Assess the morphology of the erythrocytes.
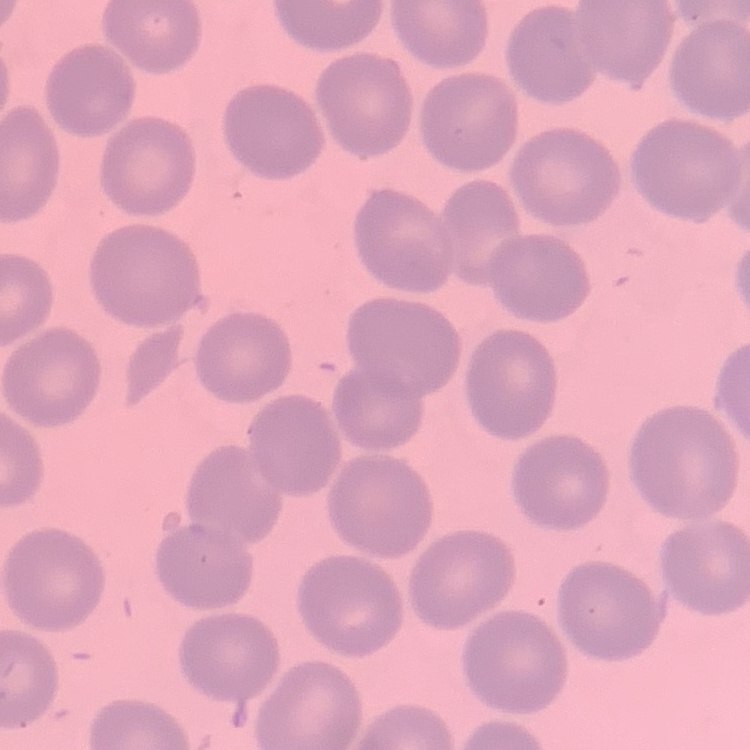

They show no rouleaux formation.

image type = one tile cut from a larger photomicrograph
preparation = thin blood film
stain = Field's or Giemsa